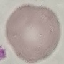

Malaria status: uninfected. Thin smear of blood. Giemsa-stained preparation. Cell patch, automatically extracted from a larger field of view and resized to 64 × 64 pixels. Photographed with a smartphone camera at the microscope eyepiece.